Assess this cell for malaria.
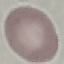
Uninfected.

image type = automatically extracted cell patch, resized to 64 × 64 pixels
stain = Giemsa
capture = smartphone camera at the microscope eyepiece
preparation = thin blood smear